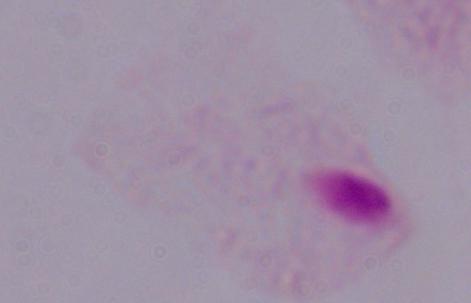

Summary:
  - Modality: photomicrograph
  - Magnification: 1000x
  - Identification: trichomonad